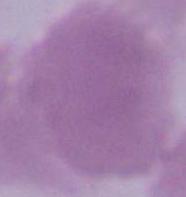

identification = red blood cell
magnification = 1000x
modality = photomicrograph